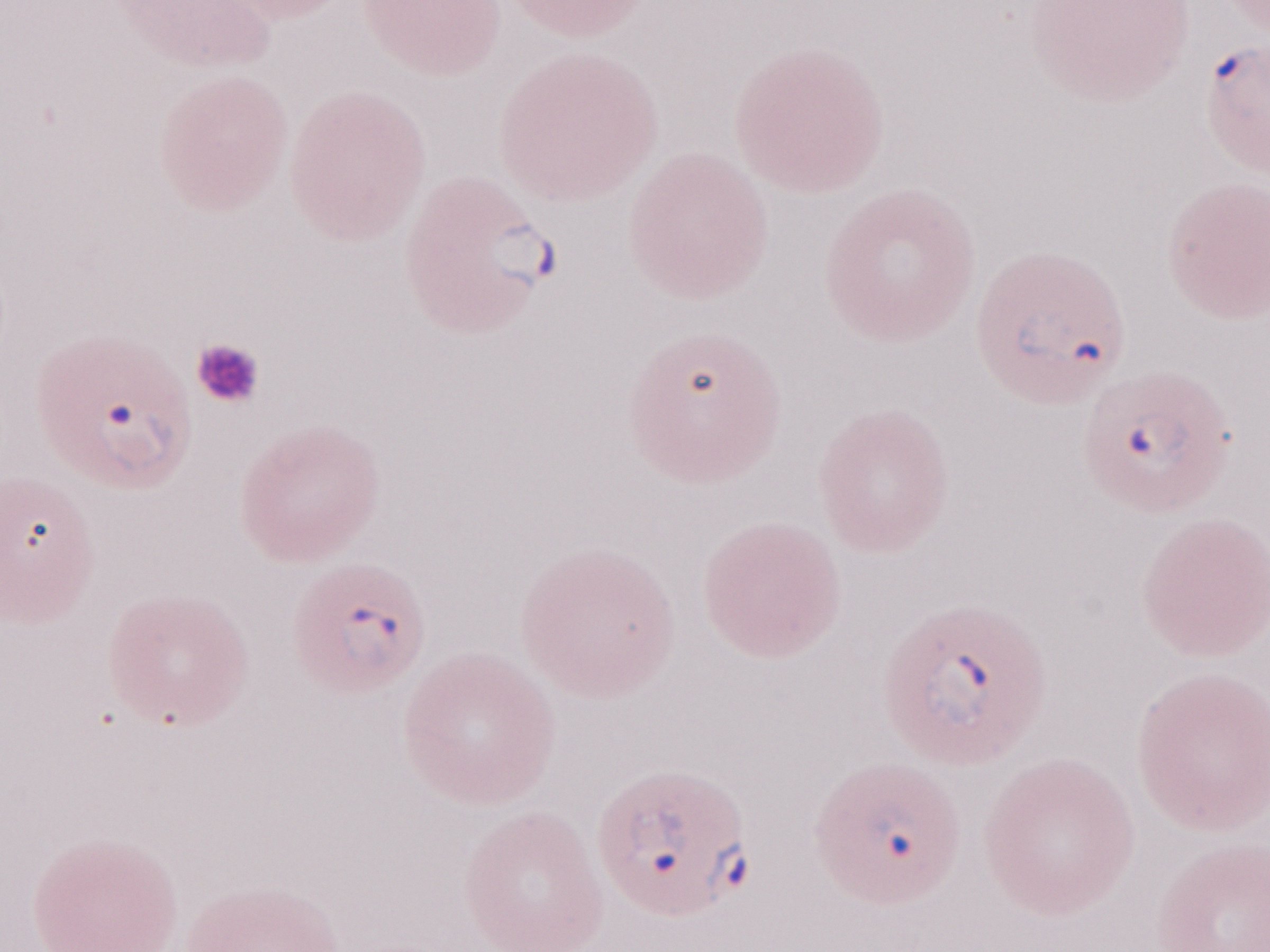
May-Grünwald-Giemsa stain. Magnification: 1,000x. Malaria diagnosis (patient-level): positive. Olympus BX43 microscope and DP73 digital camera. Thin blood film. Image is 1270×952 pixels. One field of this slide.